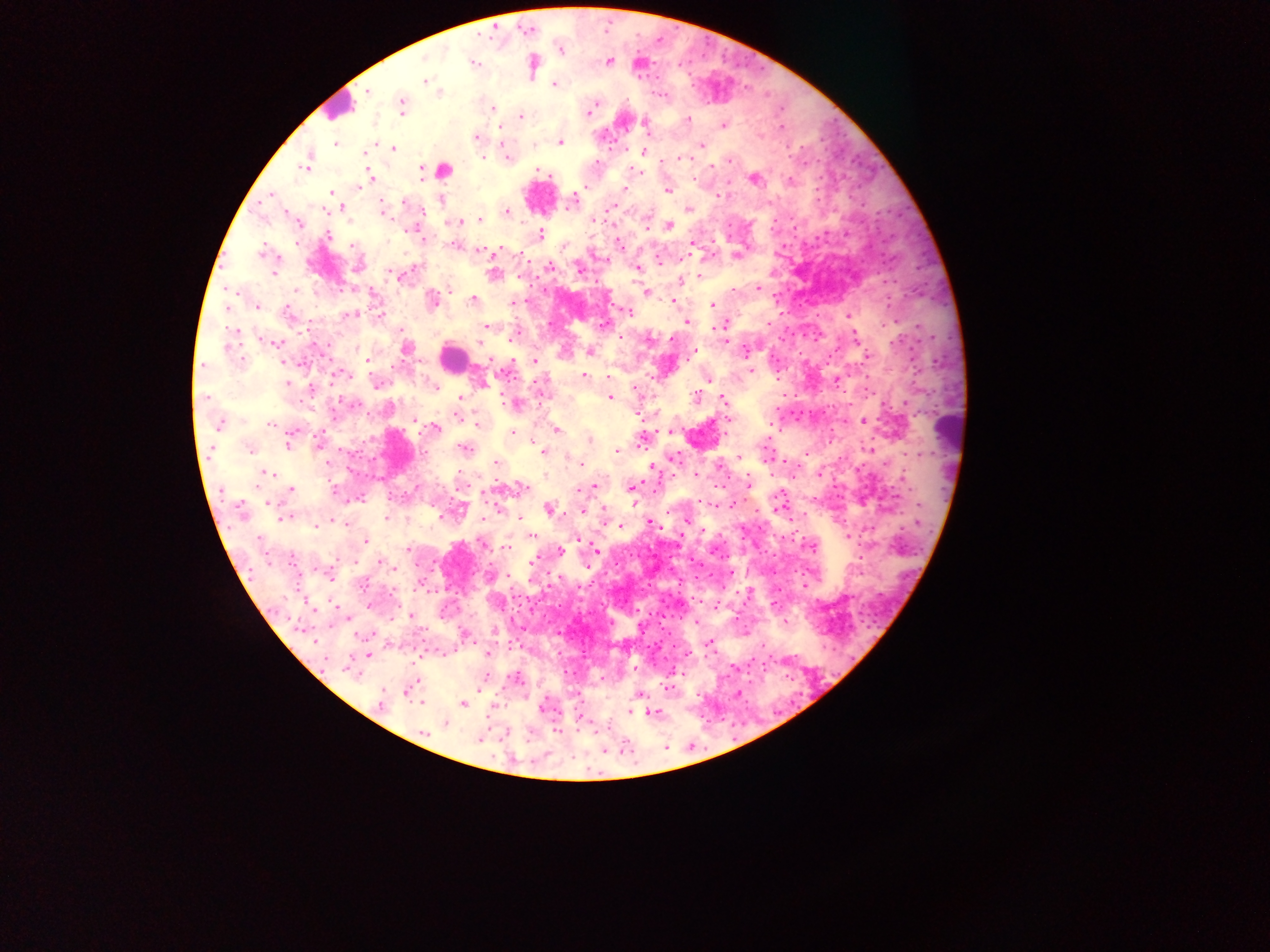

field of view = single
malaria parasite locations = approximate centers as {x, y} in pixels: {559, 50}, {425, 59}, {472, 61}, {607, 61}, {533, 65}, {424, 81}, {554, 83}, {366, 91}, {440, 91}, {401, 106}, {493, 107}, {589, 110}, {521, 116}, {687, 120}, {722, 125}, {646, 126}, {475, 137}, {559, 141}, {336, 144}, {701, 145}, {393, 148}, {365, 152}, {643, 153}, {506, 155}, {482, 157}, {680, 158}, {728, 160}, {308, 161}, {663, 161}, {535, 170}, {369, 173}, {753, 178}, {789, 180}, {357, 187}, {624, 188}, {666, 189}, {271, 193}, {331, 194}, {441, 200}, {572, 201}, {612, 205}, {342, 207}, {688, 209}, {506, 210}, {382, 211}, {344, 212}, {479, 218}, {475, 220}, {457, 221}, {669, 225}, {540, 234}, {327, 235}, {423, 241}, {693, 243}, {618, 244}, {479, 250}, {263, 253}, {737, 255}, {659, 260}, {356, 266}, {549, 266}, {578, 267}, {637, 268}, {275, 273}, {493, 274}, {401, 275}, {698, 276}, {681, 280}, {450, 288}, {757, 288}, {645, 291}, {473, 300}, {431, 301}, {672, 302}, {513, 303}, {712, 305}, {227, 306}, {257, 306}, {628, 312}, {287, 313}, {350, 314}, {847, 315}, {686, 322}, {725, 324}, {602, 325}, {487, 326}, {714, 327}, {856, 337}, {274, 342}, {725, 343}, {405, 347}, {745, 350}, {590, 351}, {692, 354}, {367, 359}, {534, 361}, {751, 370}, {336, 374}, {583, 376}, {606, 377}, {707, 378}, {376, 382}, {482, 383}, {288, 384}, {433, 386}, {312, 389}, {634, 389}, {610, 397}, {695, 397}, {722, 397}, {459, 398}, {514, 404}, {458, 417}, {863, 422}, {271, 423}, {220, 424}, {477, 424}, {434, 427}, {556, 430}, {671, 432}, {292, 433}, {512, 433}, {589, 438}, {640, 441}, {289, 443}, {319, 443}, {464, 448}, {249, 449}, {869, 449}, {617, 450}, {544, 451}, {740, 457}, {674, 458}, {496, 463}, {581, 464}, {652, 465}, {718, 465}, {266, 473}, {696, 473}, {748, 482}, {631, 486}, {522, 487}, {591, 487}, {577, 488}, {290, 489}, {361, 498}, {733, 503}, {548, 509}, {582, 511}, {240, 512}, {285, 516}, {386, 517}, {520, 519}, {686, 520}, {344, 522}, {650, 522}, {315, 526}, {621, 526}, {530, 536}, {365, 540}, {482, 543}, {506, 548}, {408, 549}, {595, 549}, {560, 551}, {534, 560}, {391, 564}, {587, 565}, {730, 573}, {410, 615}, {694, 621}, {785, 624}, {464, 634}, {314, 641}, {708, 644}, {487, 653}, {368, 654}, {350, 670}, {515, 678}, {409, 688}, {666, 688}, {736, 693}, {638, 694}, {422, 700}, {380, 703}, {464, 703}, {631, 711}, {652, 712}, {444, 724}, {422, 733}, {479, 739}
preparation = thick blood film
image size = 1270×952 pixels
country = Ghana
capture = mobile-phone photograph through a microscope
leukocyte locations = approximate centers as {x, y} in pixels: {338, 107}, {442, 169}, {538, 195}, {453, 358}, {953, 428}, {399, 450}